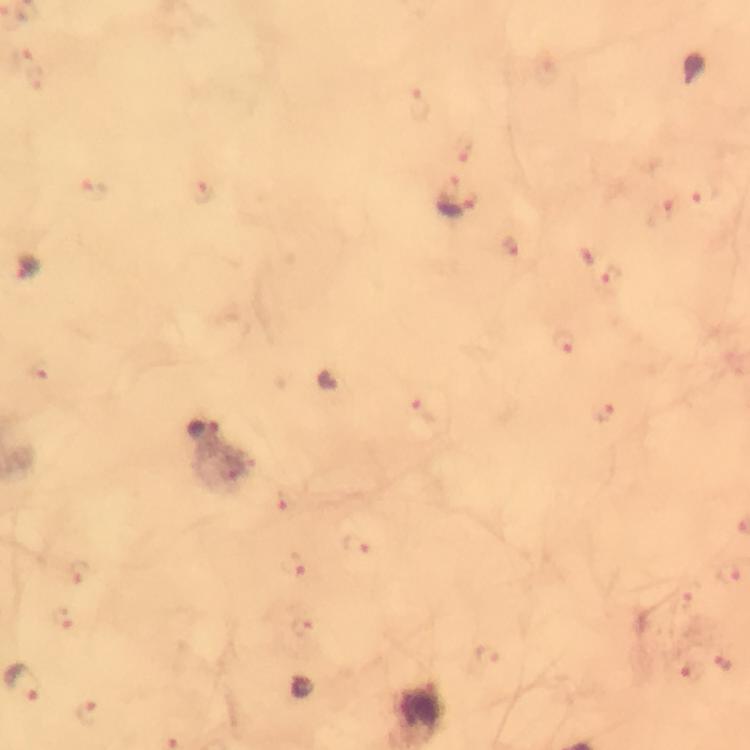

{
  "magnification": "100x",
  "context": "from a diagnostic examination for malaria",
  "immersion_oil": "used",
  "malaria_parasite_locations": "approximate centers as [x, y] in pixels: [695, 69], [456, 207], [27, 268], [566, 342], [331, 380], [202, 430], [722, 663], [303, 688]",
  "capture": "smartphone mounted on the microscope",
  "stain": "Giemsa",
  "preparation": "thick blood smear",
  "cropped_from": "a single field of view",
  "image_size": "750×750 pixels"
}